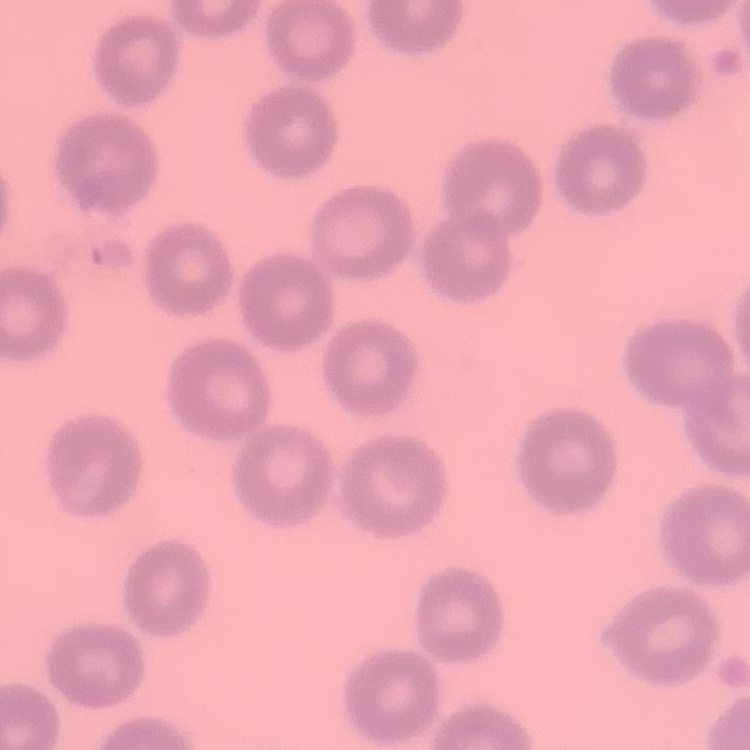

Summary:
  - Erythrocyte morphology: no rouleaux formation
  - Image type: one tile cut from a larger photomicrograph
  - Stain: Field's or Giemsa
  - Preparation: thin peripheral smear